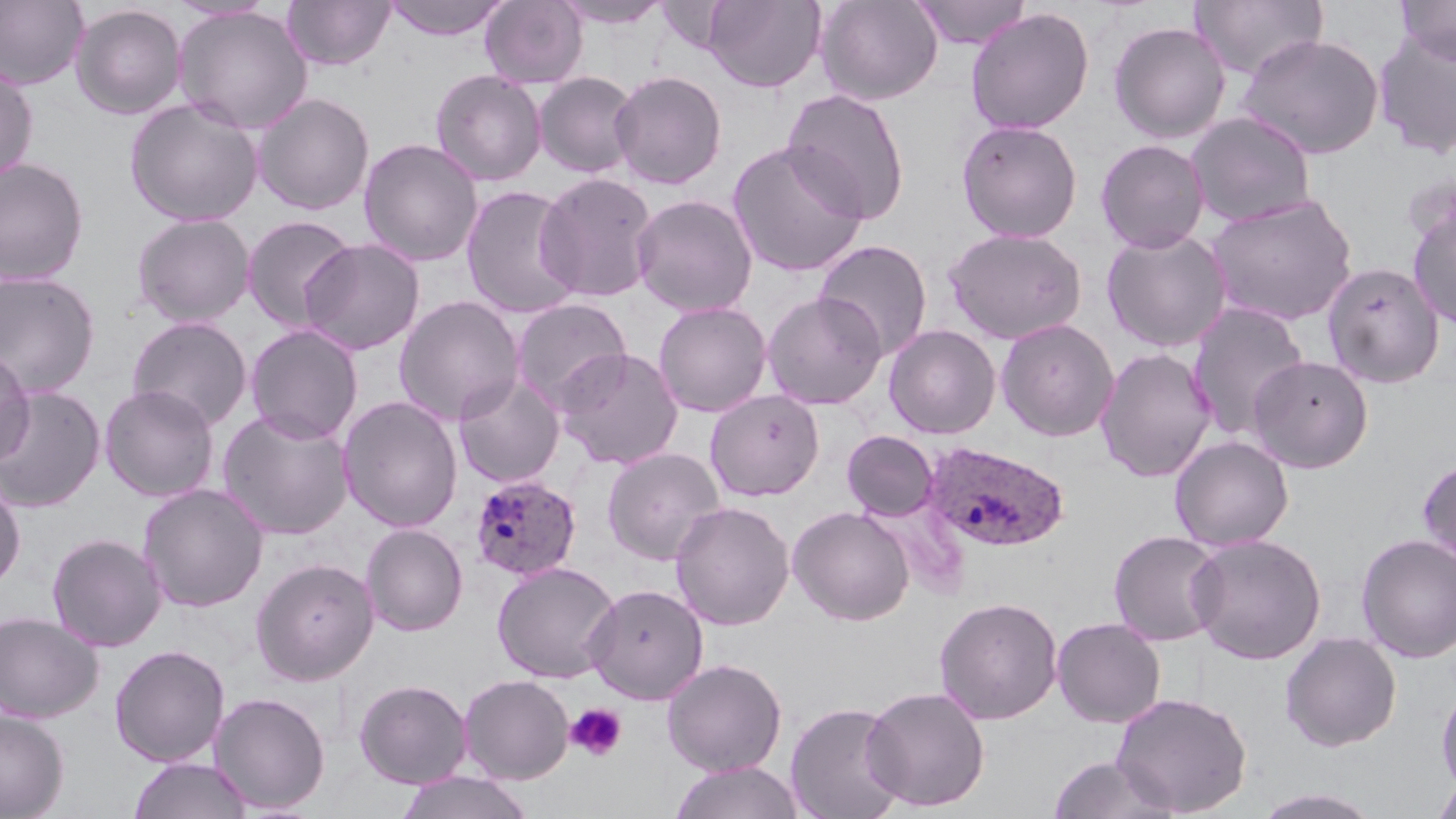 Approximate bounding boxes as (x1,y1)-(x2,y2) corner pairs in pixels. Platelet locations: (565,703)-(628,762). Plasmodium ovale-infected red blood cell locations: (921,439)-(1071,552), (469,474)-(582,582). Uninfected red blood cell locations: (0,0)-(90,91), (282,0)-(395,71), (384,0)-(510,41), (480,0)-(588,89), (702,0)-(826,92), (816,0)-(943,106), (912,0)-(1031,49), (1190,0)-(1329,81), (1394,0)-(1456,65), (552,1)-(673,30), (70,4)-(187,120), (173,6)-(313,135), (965,7)-(1094,135), (1108,21)-(1231,143), (1372,27)-(1456,159), (1236,33)-(1385,159), (0,64)-(38,183), (430,69)-(547,186), (610,70)-(727,190), (534,71)-(640,178), (781,88)-(911,225), (253,92)-(375,216), (124,98)-(264,227), (1186,111)-(1316,228), (957,119)-(1083,243), (358,138)-(484,267), (1095,139)-(1210,253), (727,141)-(868,277), (0,157)-(90,285), (535,172)-(658,303), (461,184)-(584,320), (1204,192)-(1358,327), (631,194)-(758,317), (1407,202)-(1456,330), (131,213)-(256,327), (241,214)-(360,333), (943,227)-(1087,344), (1101,227)-(1233,353), (299,237)-(426,356), (813,240)-(932,361), (1321,261)-(1446,388), (1,271)-(101,398), (762,291)-(887,410), (393,295)-(525,425), (509,298)-(633,411), (653,301)-(773,418), (1186,302)-(1310,442), (126,316)-(253,431), (995,318)-(1120,442), (244,324)-(364,444), (883,324)-(1002,438), (554,347)-(684,469), (1096,347)-(1217,483), (0,349)-(35,468), (1247,354)-(1374,473), (452,373)-(566,488), (99,384)-(220,502), (1,386)-(106,512), (705,390)-(824,501), (338,396)-(464,532), (216,408)-(355,540), (841,430)-(940,521), (1170,435)-(1294,551), (601,447)-(726,566), (1417,456)-(1456,567), (0,476)-(26,593), (137,483)-(269,612), (670,501)-(795,630), (787,505)-(915,626), (361,523)-(468,636), (1108,530)-(1227,646), (46,532)-(167,652), (1187,533)-(1327,665), (1356,533)-(1456,663), (250,557)-(379,686), (491,561)-(621,683), (584,583)-(709,704), (933,596)-(1063,725), (0,611)-(104,723), (1051,617)-(1166,727), (1280,631)-(1402,752), (109,644)-(230,767), (661,658)-(787,776), (458,674)-(575,784), (354,679)-(473,788), (1435,683)-(1456,796), (861,685)-(991,812), (209,691)-(331,813), (1110,691)-(1253,816), (785,701)-(907,819), (0,710)-(69,818), (1046,753)-(1180,819), (127,756)-(253,818), (669,761)-(805,819), (395,770)-(535,819), (1430,776)-(1456,818), (1254,786)-(1387,818). Slide-level diagnosis: Plasmodium ovale. Captured at 1000x magnification. Image is 1456×819 pixels. Thin blood film. May-Grünwald-Giemsa stain. One field of a larger specimen. Optical microscopy.